Point out each malaria parasite.
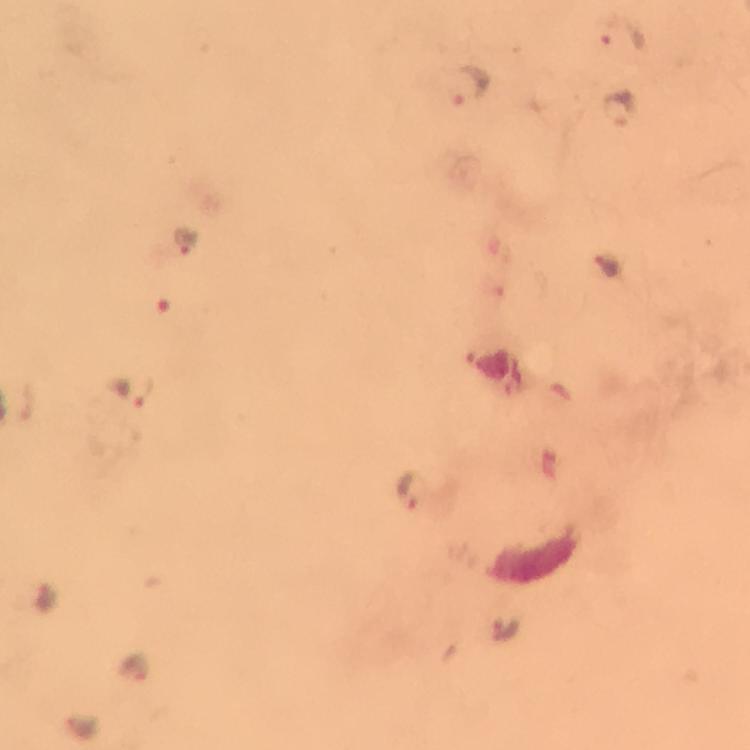
Approximate centers as {x, y} in pixels.
Malaria parasites: {621, 33}, {472, 85}, {618, 104}, {183, 241}, {607, 267}, {131, 391}, {410, 493}, {506, 628}, {81, 724}.

Photographed through the microscope with a smartphone camera. Image is 750×750 pixels. At 100x magnification. Immersion oil applied. Thick smear. Giemsa stain. From a malaria diagnostic workup. A crop from one field of view.